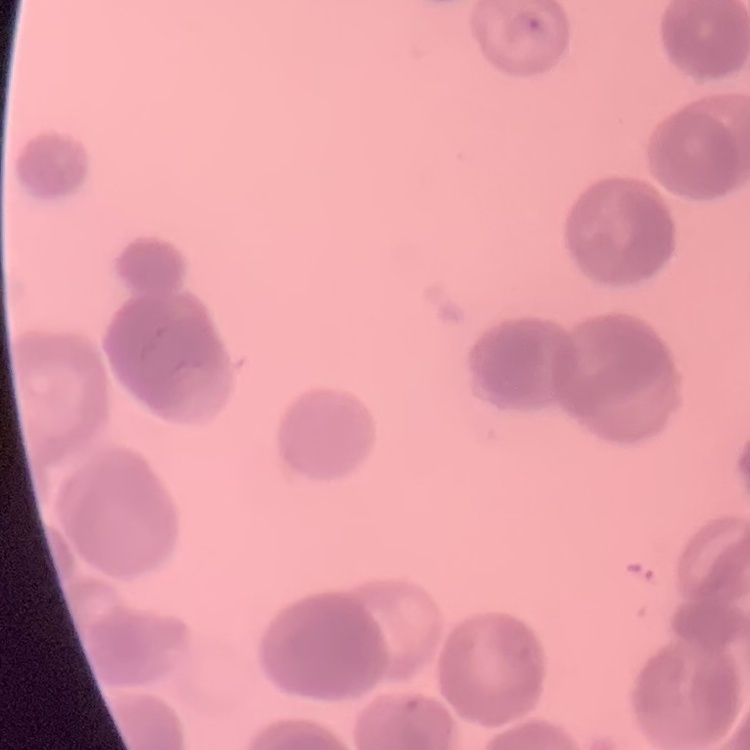
Summary:
  - Red blood cell morphology: rouleaux formation
  - Preparation: thin peripheral smear
  - Image type: one tile cut from a larger photomicrograph
  - Stain: Field's or Giemsa